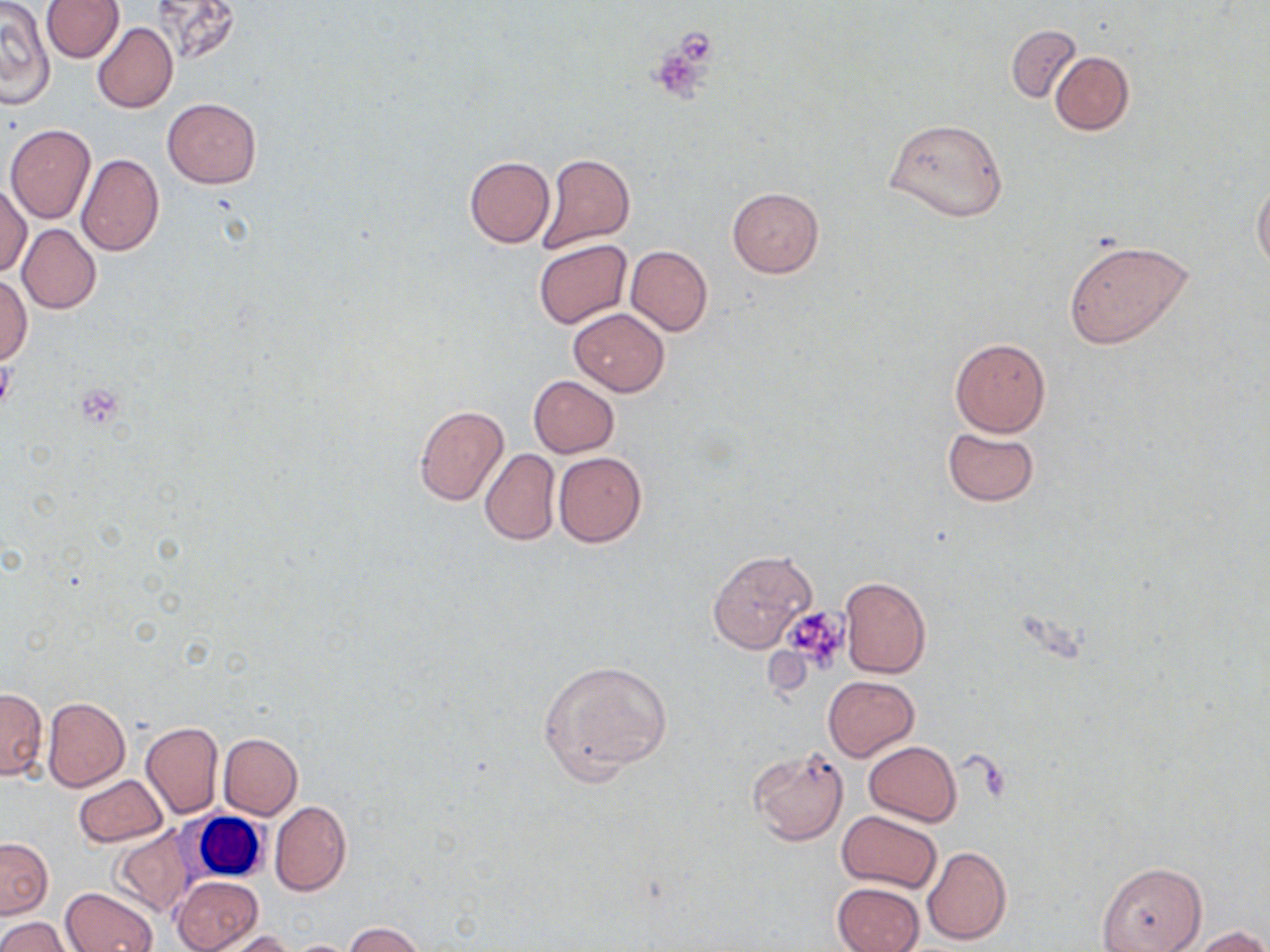

Summary:
  - Coordinate format: approximate bounding boxes as [x1, y1, x2, y2] in pixels
  - White blood cell locations: [173, 804, 274, 886]
  - Uninfected red blood cell locations: [40, 0, 124, 63], [150, 0, 246, 64], [1, 2, 55, 108], [92, 22, 177, 114], [1005, 25, 1082, 104], [1049, 50, 1134, 135], [162, 98, 260, 189], [884, 116, 1008, 222], [5, 122, 95, 224], [76, 152, 164, 255], [536, 153, 636, 254], [465, 156, 555, 248], [1252, 180, 1270, 273], [0, 182, 31, 277], [727, 188, 823, 278], [18, 224, 100, 313], [1063, 238, 1195, 350], [534, 240, 632, 329], [626, 245, 712, 336], [0, 276, 31, 363], [569, 309, 668, 396], [950, 337, 1052, 437], [529, 376, 619, 457], [414, 405, 510, 507], [942, 427, 1041, 505], [479, 448, 560, 545], [552, 452, 647, 548], [708, 549, 817, 653], [840, 577, 931, 678], [537, 658, 672, 782], [822, 674, 919, 761], [0, 688, 47, 779], [42, 696, 130, 792], [141, 720, 224, 819], [218, 732, 302, 818], [863, 741, 961, 827], [747, 745, 850, 846], [74, 773, 167, 846], [271, 801, 351, 896], [836, 810, 942, 894], [110, 825, 198, 917], [0, 837, 53, 918], [923, 845, 1011, 944], [1096, 861, 1205, 951], [172, 876, 264, 952], [832, 881, 924, 952], [61, 887, 158, 952], [0, 917, 68, 952], [345, 922, 423, 951], [1194, 926, 1270, 952], [220, 931, 299, 952]
  - Platelet locations: [645, 39, 718, 103], [75, 385, 122, 425], [781, 606, 852, 672]
  - Slide-level diagnosis: negative for blood parasites
  - Magnification: 1000x
  - Image size: 1270×952 pixels
  - Stain: May-Grünwald-Giemsa
  - Modality: light microscopy
  - Field of view: single
  - Preparation: thin blood film